Report the malaria status of this cell.
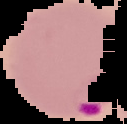

Parasitized.

Summary:
  - Image type: segmented cell region with the area outside set to black
  - Preparation: thin blood film
  - Image size: 127×124 pixels